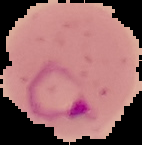
{
  "preparation": "thin blood smear",
  "malaria_status": "parasitized",
  "image_size": "142×145 pixels",
  "image_type": "segmented cell region on a black background"
}